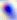 400x magnification. Toxoplasma gondii is seen. Photomicrograph.